Assess for Plasmodium parasites.
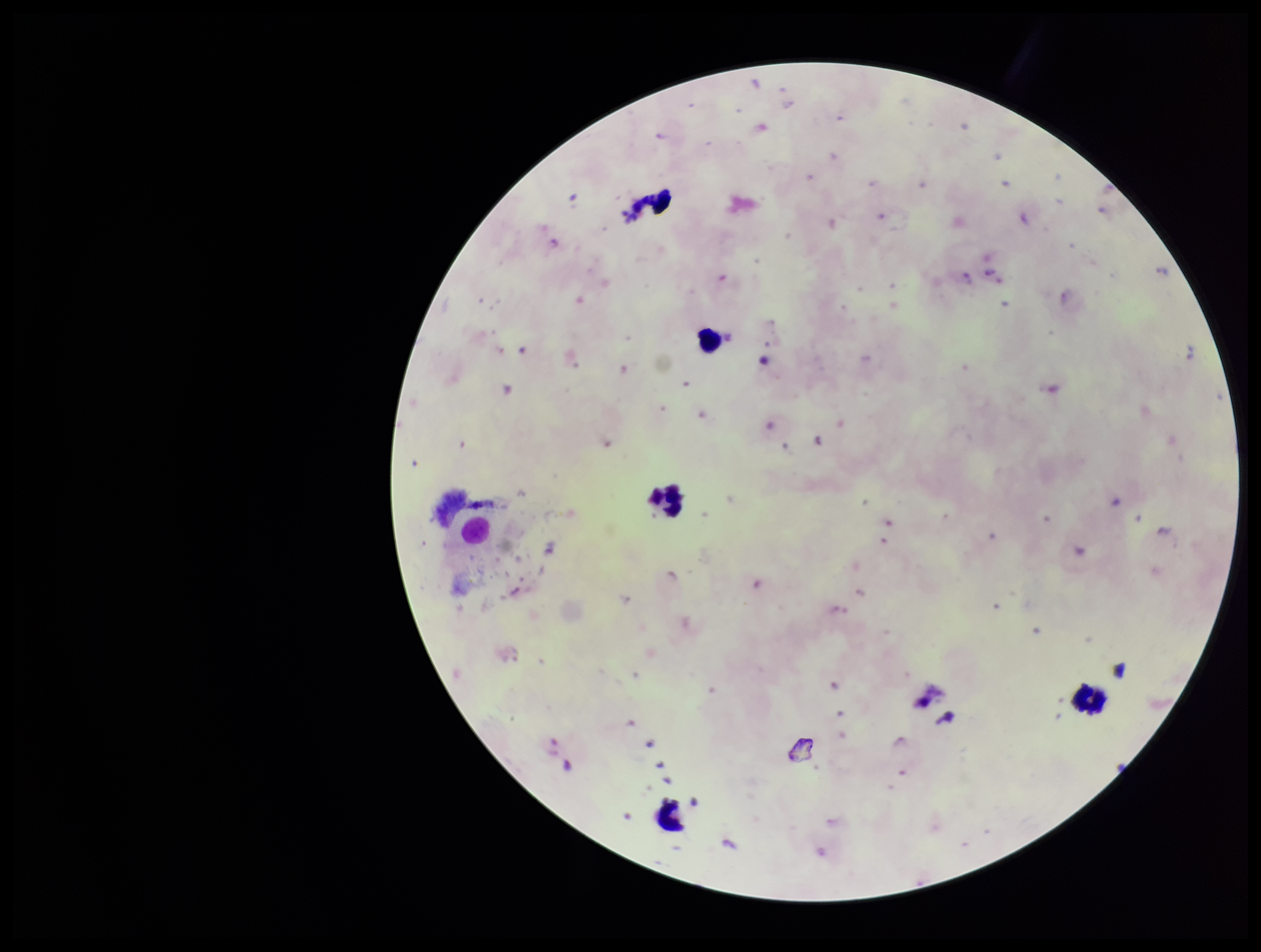

Seen.

{
  "species_reported_for_this_patient": "Plasmodium falciparum",
  "stain": "Giemsa",
  "parasite_count": 14,
  "preparation": "thick smear",
  "capture": "smartphone photograph through the microscope eyepiece",
  "leukocyte_count": 5,
  "field_of_view": "one from this slide",
  "image_size": "1261×952 pixels",
  "patient_malaria_status": "infected"
}